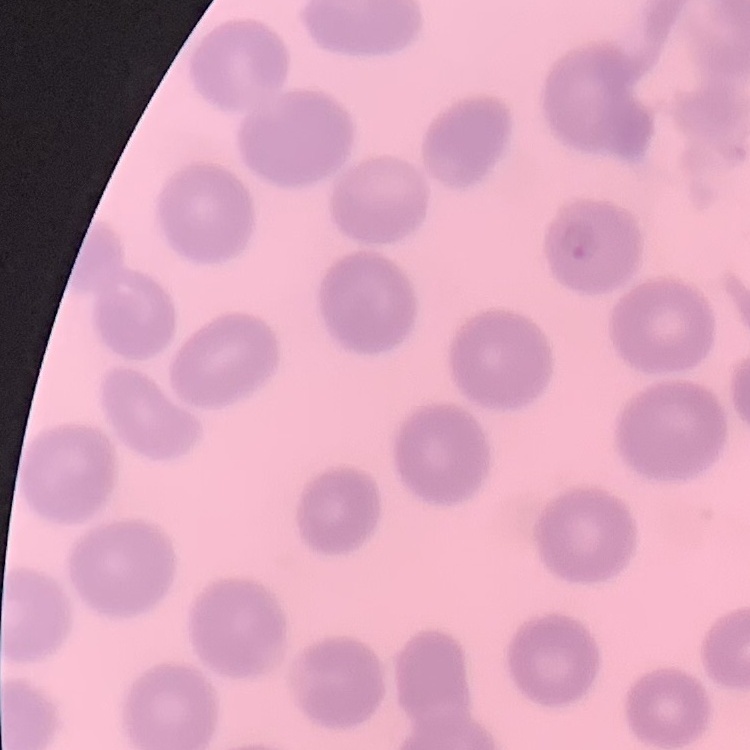
Summary:
  - Erythrocyte morphology: no rouleaux formation
  - Image type: one tile cut from a larger photomicrograph
  - Preparation: thin peripheral smear
  - Stain: Field's or Giemsa